State the blood parasite species.
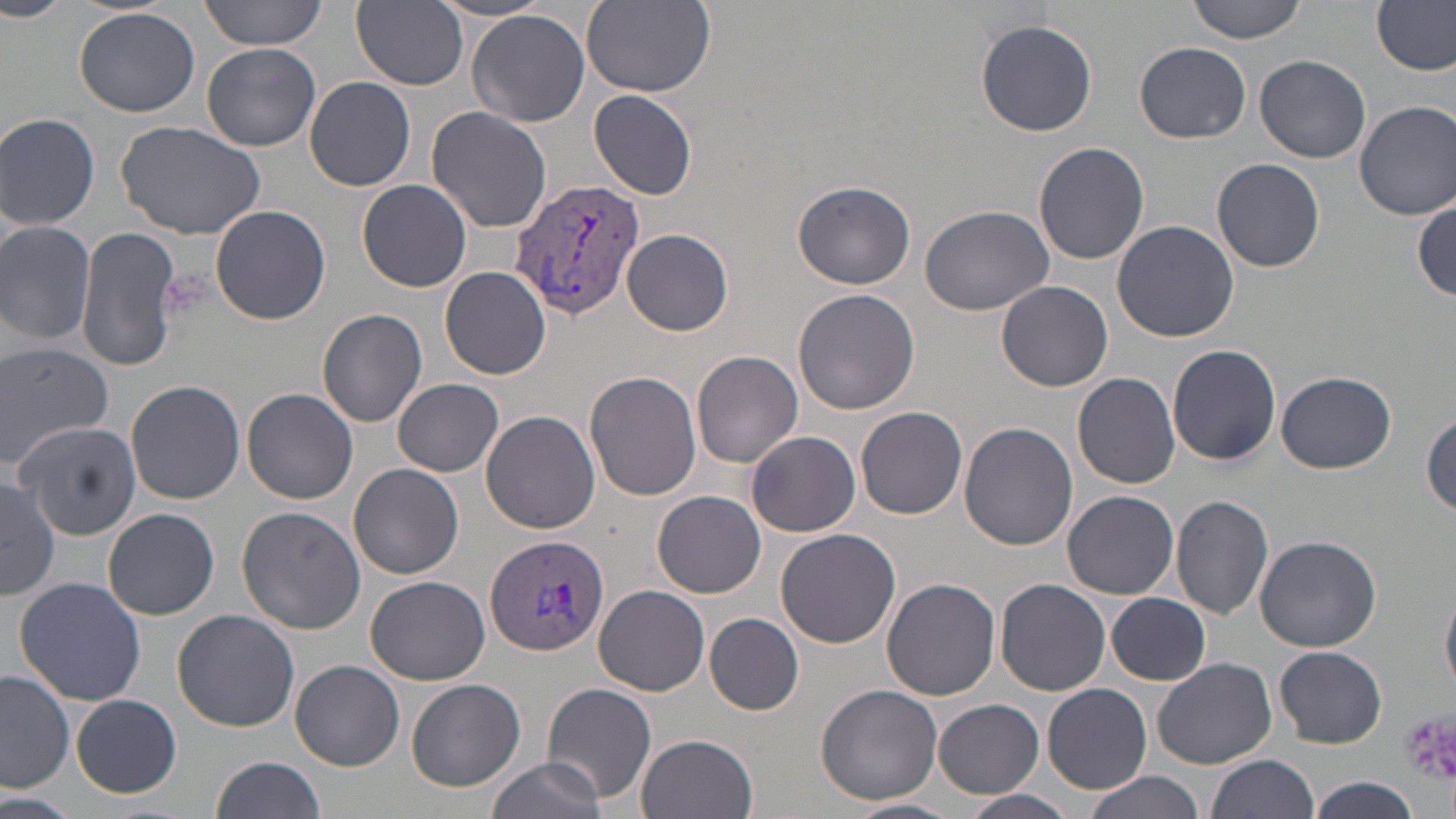

Plasmodium vivax.

Summary:
  - Coordinate format: approximate bounding boxes as named x1/y1/x2/y2 corners in pixels
  - Uninfected red blood cell locations: (x1=0, y1=0, x2=69, y2=21), (x1=200, y1=0, x2=329, y2=50), (x1=580, y1=0, x2=716, y2=97), (x1=1187, y1=0, x2=1308, y2=43), (x1=1373, y1=0, x2=1454, y2=76), (x1=352, y1=1, x2=468, y2=89), (x1=73, y1=6, x2=203, y2=117), (x1=468, y1=10, x2=590, y2=128), (x1=975, y1=18, x2=1097, y2=136), (x1=1136, y1=41, x2=1251, y2=143), (x1=202, y1=42, x2=321, y2=151), (x1=1254, y1=55, x2=1372, y2=164), (x1=305, y1=76, x2=416, y2=191), (x1=590, y1=90, x2=697, y2=200), (x1=1355, y1=101, x2=1456, y2=221), (x1=426, y1=106, x2=551, y2=232), (x1=0, y1=112, x2=101, y2=228), (x1=118, y1=118, x2=265, y2=240), (x1=1035, y1=142, x2=1150, y2=264), (x1=1212, y1=158, x2=1325, y2=271), (x1=357, y1=178, x2=472, y2=292), (x1=791, y1=178, x2=914, y2=290), (x1=1413, y1=195, x2=1454, y2=299), (x1=919, y1=204, x2=1055, y2=315), (x1=212, y1=205, x2=330, y2=324), (x1=1111, y1=220, x2=1240, y2=342), (x1=0, y1=221, x2=98, y2=347), (x1=76, y1=227, x2=183, y2=373), (x1=623, y1=230, x2=732, y2=335), (x1=440, y1=266, x2=551, y2=380), (x1=996, y1=281, x2=1114, y2=393), (x1=793, y1=289, x2=920, y2=415), (x1=318, y1=307, x2=427, y2=428), (x1=0, y1=341, x2=113, y2=465), (x1=1167, y1=343, x2=1282, y2=466), (x1=692, y1=350, x2=804, y2=468), (x1=585, y1=371, x2=701, y2=501), (x1=1278, y1=371, x2=1394, y2=472), (x1=1073, y1=372, x2=1181, y2=490), (x1=394, y1=378, x2=504, y2=475), (x1=125, y1=380, x2=245, y2=505), (x1=243, y1=388, x2=358, y2=505), (x1=856, y1=405, x2=968, y2=519), (x1=1422, y1=408, x2=1456, y2=519), (x1=480, y1=410, x2=600, y2=534), (x1=18, y1=422, x2=144, y2=539), (x1=960, y1=422, x2=1078, y2=551), (x1=747, y1=430, x2=861, y2=537), (x1=350, y1=464, x2=463, y2=580), (x1=2, y1=477, x2=58, y2=600), (x1=653, y1=490, x2=766, y2=598), (x1=1064, y1=491, x2=1178, y2=600), (x1=1172, y1=494, x2=1274, y2=619), (x1=236, y1=504, x2=368, y2=634), (x1=101, y1=507, x2=219, y2=620), (x1=775, y1=528, x2=901, y2=648), (x1=1255, y1=535, x2=1383, y2=652), (x1=13, y1=577, x2=148, y2=705), (x1=365, y1=577, x2=491, y2=684), (x1=882, y1=577, x2=1000, y2=700), (x1=995, y1=579, x2=1111, y2=696), (x1=1441, y1=583, x2=1456, y2=698), (x1=594, y1=586, x2=710, y2=696), (x1=1107, y1=592, x2=1211, y2=684), (x1=172, y1=609, x2=299, y2=732), (x1=705, y1=613, x2=804, y2=715), (x1=1274, y1=646, x2=1387, y2=748), (x1=1151, y1=657, x2=1277, y2=767), (x1=292, y1=659, x2=404, y2=770), (x1=0, y1=670, x2=76, y2=793), (x1=405, y1=677, x2=524, y2=791), (x1=541, y1=682, x2=655, y2=804), (x1=1043, y1=683, x2=1152, y2=794), (x1=815, y1=684, x2=944, y2=806), (x1=72, y1=694, x2=182, y2=797), (x1=934, y1=699, x2=1043, y2=797), (x1=636, y1=733, x2=758, y2=819), (x1=210, y1=755, x2=327, y2=819), (x1=1207, y1=755, x2=1318, y2=819), (x1=485, y1=756, x2=611, y2=819), (x1=1081, y1=771, x2=1203, y2=819), (x1=1304, y1=776, x2=1423, y2=818), (x1=955, y1=792, x2=1076, y2=819), (x1=0, y1=794, x2=74, y2=819), (x1=846, y1=798, x2=962, y2=819)
  - Plasmodium vivax-infected red blood cell locations: (x1=511, y1=175, x2=645, y2=321), (x1=484, y1=532, x2=609, y2=657)
  - Platelet locations: (x1=1399, y1=707, x2=1456, y2=788)
  - Image size: 1456×819 pixels
  - Stain: May-Grünwald-Giemsa
  - Magnification: 1000x
  - Field of view: single
  - Preparation: thin blood smear
  - Modality: optical microscopy